Assess this cell for malaria.
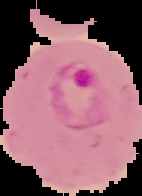
Parasitized.

preparation = thin blood film
image type = segmented cell region on a black background
image size = 142×196 pixels